Assess this cell for malaria.
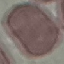
It is uninfected.

preparation = thin blood film
image type = automatically extracted cell patch, resized to 64 × 64 pixels
stain = Giemsa
capture = smartphone through the microscope eyepiece